State the preparation type.
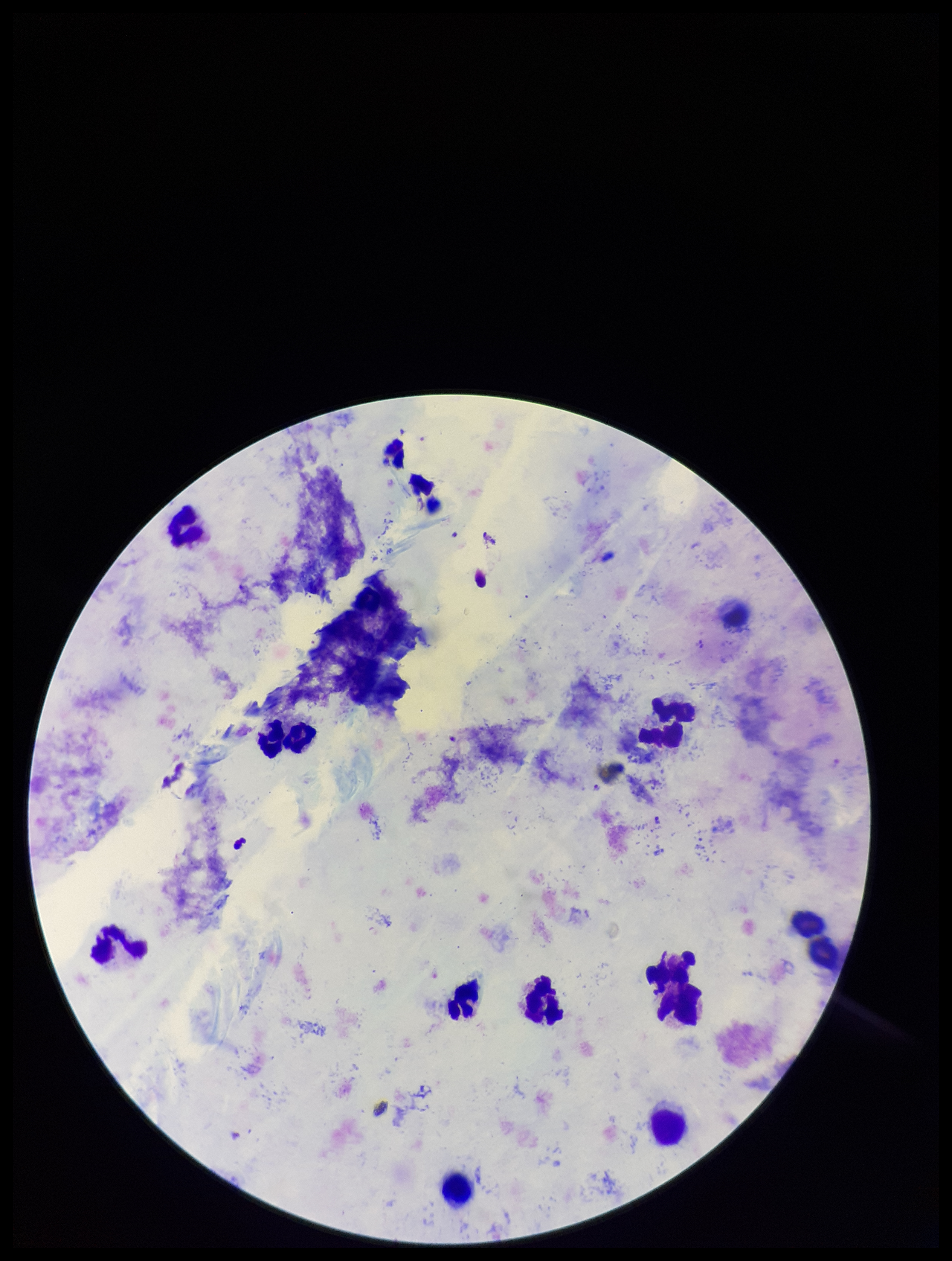
It is a thick blood smear.

Summary:
  - Patient malaria status: infected
  - Leukocyte count: 14
  - Species reported for this patient: Plasmodium falciparum
  - Field of view: single
  - Parasite count: 2
  - Stain: Giemsa
  - Plasmodium parasites: seen
  - Capture: smartphone photograph through the microscope eyepiece
  - Image size: 952×1261 pixels